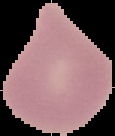

Result: no Plasmodium parasites seen. From a thin blood smear. Segmented cell region on a black background. Image is 115×136 pixels.